Report the malaria status of this cell.
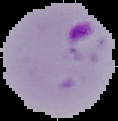
It is parasitized.

Image is 118×121 pixels. Segmented cell region on a black background. From a thin blood smear.